Classify this cell by malaria status.
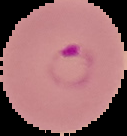

It is parasitized.

image type = segmented cell region on a black background
preparation = thin blood film
image size = 127×136 pixels